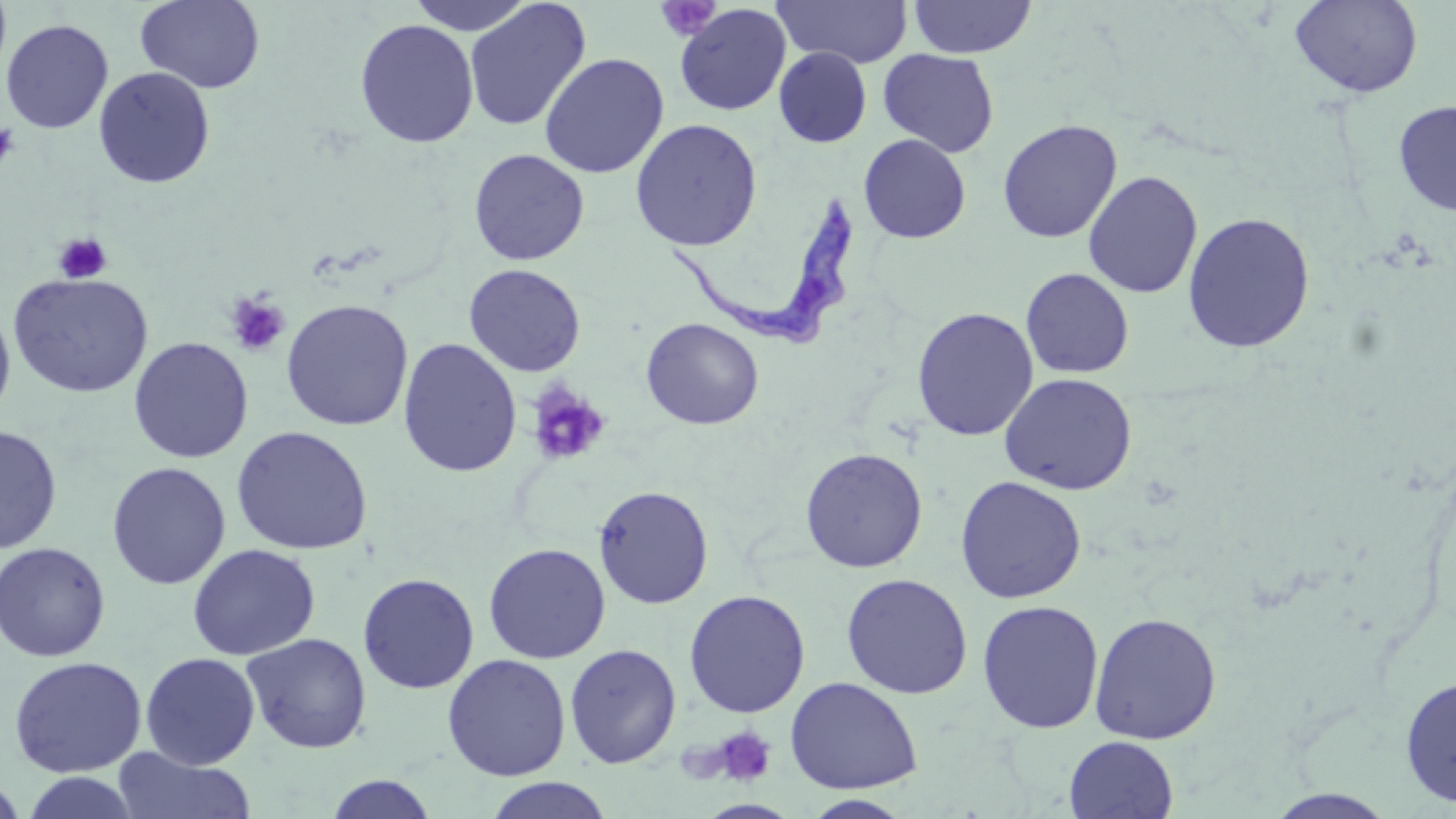
Approximate bounding boxes as [x1, y1, x2, y2] in pixels. Trypanosoma brucei locations: [664, 194, 859, 354]. Uninfected red blood cell locations: [405, 0, 538, 35], [464, 0, 591, 131], [773, 0, 913, 68], [1289, 0, 1423, 99], [135, 1, 265, 94], [907, 1, 1037, 59], [674, 3, 792, 116], [1, 19, 114, 134], [355, 19, 479, 148], [774, 47, 872, 148], [878, 49, 999, 157], [538, 53, 669, 178], [93, 67, 216, 189], [1393, 99, 1456, 215], [629, 118, 763, 251], [997, 119, 1122, 244], [859, 134, 971, 243], [468, 149, 590, 266], [1083, 170, 1203, 298], [1182, 212, 1316, 353], [463, 264, 586, 377], [1021, 269, 1134, 379], [8, 273, 153, 398], [280, 299, 414, 431], [0, 303, 16, 424], [912, 307, 1038, 441], [641, 317, 764, 430], [128, 337, 253, 463], [397, 337, 522, 478], [999, 372, 1137, 495], [0, 424, 62, 553], [230, 425, 373, 556], [799, 447, 928, 573], [106, 461, 231, 589], [954, 475, 1087, 604], [593, 485, 713, 609], [0, 541, 111, 662], [483, 542, 611, 664], [186, 543, 321, 661], [357, 572, 479, 694], [840, 573, 973, 699], [683, 589, 810, 719], [977, 599, 1104, 735], [1089, 611, 1222, 745], [241, 632, 372, 754], [564, 643, 681, 769], [140, 652, 261, 770], [442, 653, 570, 781], [7, 656, 148, 777], [1398, 673, 1456, 808], [785, 676, 923, 794], [1063, 736, 1179, 819], [111, 747, 257, 819], [20, 771, 141, 818], [322, 774, 440, 818], [0, 776, 29, 819], [484, 777, 613, 819], [1263, 789, 1399, 819], [802, 794, 913, 818]. Platelet locations: [655, 0, 722, 41], [0, 123, 20, 171], [53, 233, 112, 283], [225, 292, 291, 357], [526, 385, 609, 467], [712, 725, 778, 787]. Slide-level diagnosis: Trypanosoma brucei. Light microscopy. Image is 1456×819 pixels. May-Grünwald-Giemsa-stained preparation. Thin blood film. Captured at 1000x magnification. Single field of view.